Assess this cell for malaria.
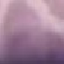
It is uninfected.

stain = Giemsa
preparation = thin blood film
image type = automatically extracted cell patch, resized to 64 × 64 pixels
capture = smartphone through the microscope eyepiece